Assess this cell for malaria.
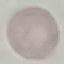

It is uninfected.

Summary:
  - Capture: smartphone camera at the microscope eyepiece
  - Preparation: thin blood smear
  - Image type: cell patch, automatically extracted from a larger field of view and resized to 64 × 64 pixels
  - Stain: Giemsa